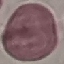
Summary:
  - Malaria status: uninfected
  - Preparation: thin smear
  - Stain: Giemsa
  - Image type: automatically extracted cell patch, resized to 64 × 64 pixels
  - Capture: smartphone camera at the microscope eyepiece